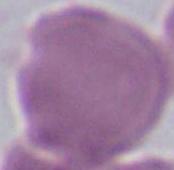
identification: erythrocyte
magnification: 1000x
modality: photomicrograph